Assess this cell for malaria.
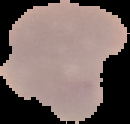
It is parasitized.

Image is 130×124 pixels. The area outside the segmented cell region is set to black. From a thin blood film.